State which parasite is depicted.
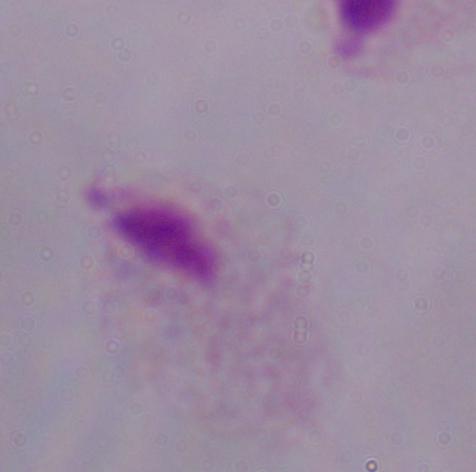

This is a trichomonad.

modality = micrograph
magnification = 1000x